Name the parasite shown.
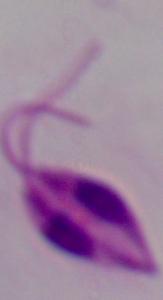
Leishmania.

1000x magnification. Micrograph.